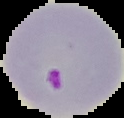
Malaria status: parasitized. Image is 124×118 pixels. Cell region segmented out of the field of view; the surrounding area is masked to black. From a thin blood smear.